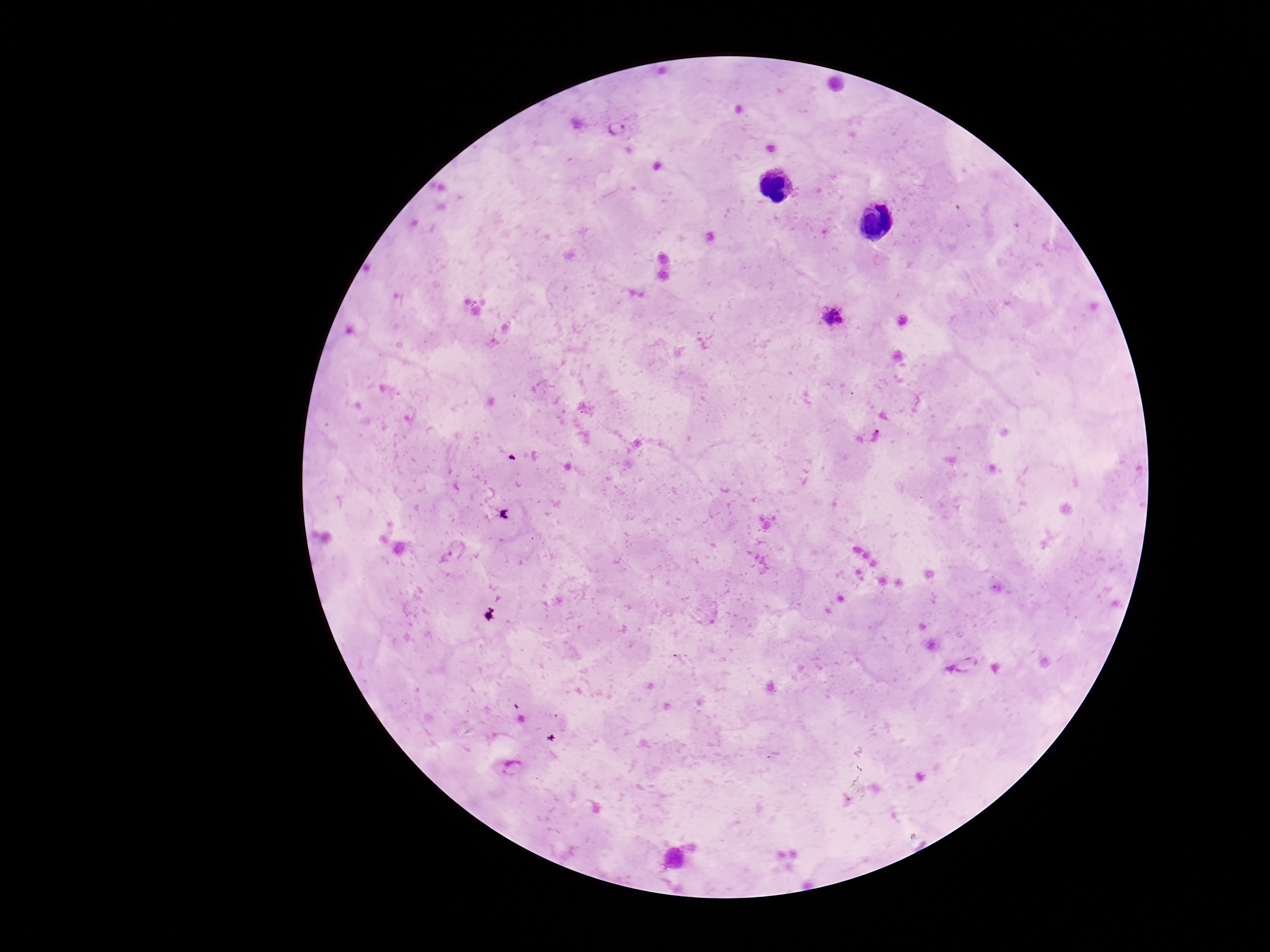
Approximate centers as (x, y) in pixels. Plasmodium parasite locations: (618, 128), (832, 317), (456, 550), (964, 665), (513, 767). Giemsa-stained preparation. Patient malaria status: infected. One field from this slide. Image is 1270×952 pixels. Photographed through the microscope eyepiece with a smartphone camera. 100x magnification. Thick blood smear.